Locate every Plasmodium ovale-infected red blood cell.
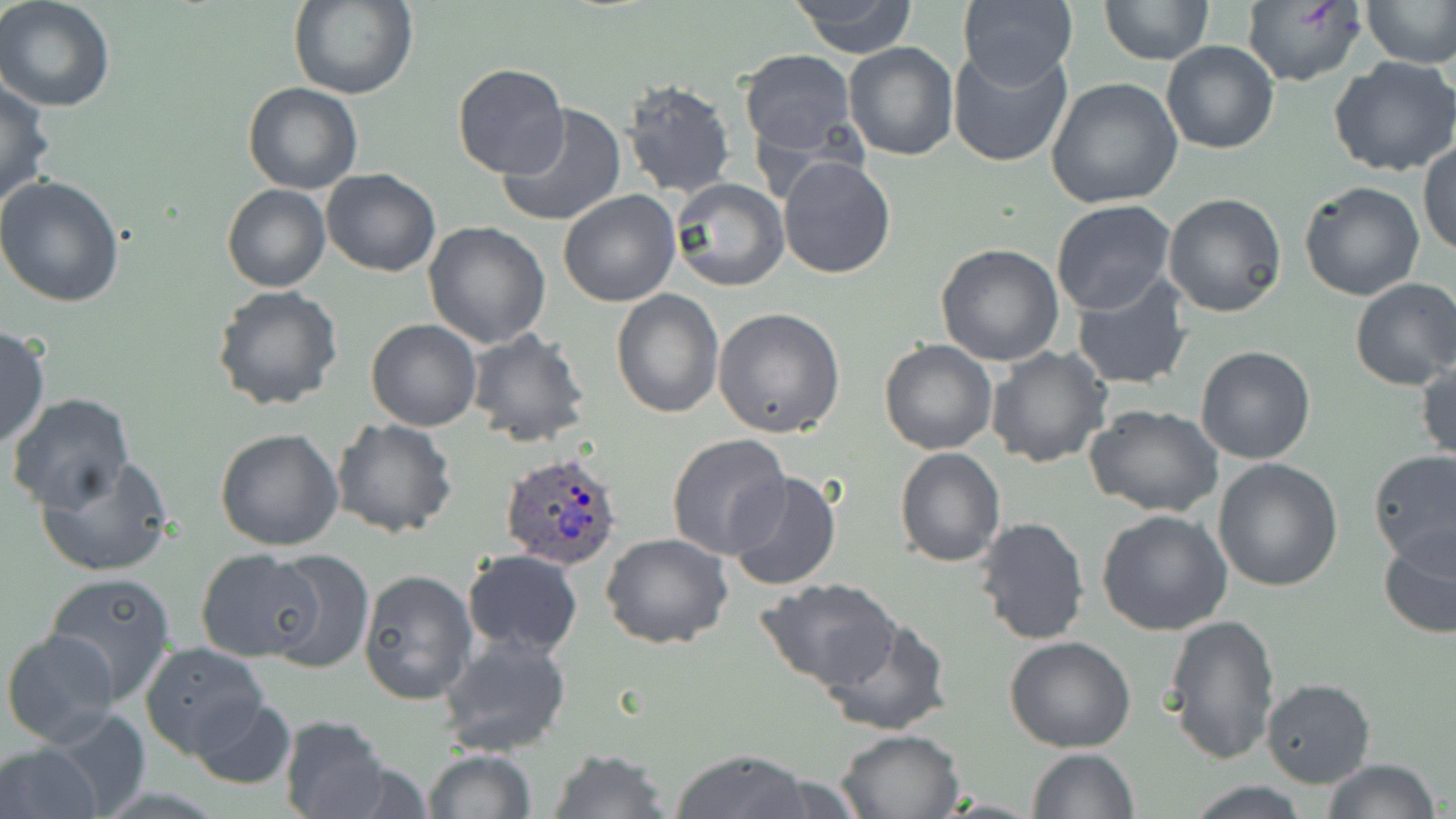

Approximate bounding boxes as (x1,y1)-(x2,y2) corner pairs in pixels.
Plasmodium ovale-infected red blood cells: (499,450)-(625,568).

slide_level_diagnosis: Plasmodium ovale
field_of_view: one of a larger specimen
preparation: thin blood smear
magnification: 1000x
stain: May-Grünwald-Giemsa
uninfected_red_blood_cell_locations: 'approximate bounding boxes as (x1,y1)-(x2,y2) corner pairs in pixels: (287,0)-(419,100), (790,0)-(919,56), (1100,0)-(1215,66), (1241,0)-(1365,86), (1365,0)-(1456,68), (0,1)-(118,113), (955,3)-(1078,84), (1161,38)-(1279,156), (843,42)-(960,161), (948,44)-(1075,168), (739,48)-(858,157), (1328,56)-(1456,176), (451,63)-(570,180), (1045,77)-(1186,209), (0,78)-(55,214), (618,78)-(737,199), (243,83)-(363,195), (496,103)-(627,228), (1419,140)-(1456,257), (777,154)-(896,279), (320,168)-(441,277), (0,173)-(126,307), (670,179)-(789,293), (1298,181)-(1425,300), (222,184)-(330,293), (558,189)-(682,307), (1162,192)-(1288,318), (1050,199)-(1178,316), (423,223)-(551,348), (935,242)-(1066,367), (1070,270)-(1196,391), (1349,278)-(1456,390), (212,285)-(346,411), (611,289)-(722,417), (713,308)-(845,438), (365,319)-(483,431), (0,324)-(49,451), (465,327)-(591,449), (879,339)-(998,455), (984,346)-(1112,468), (1194,346)-(1318,464), (1417,359)-(1455,465), (5,394)-(135,514), (1084,403)-(1225,517), (329,416)-(457,538), (215,428)-(346,551), (666,432)-(792,559), (895,447)-(1006,567), (1368,448)-(1456,566), (35,457)-(174,578), (1213,457)-(1344,592), (724,471)-(845,591), (1096,509)-(1233,636), (974,515)-(1091,645), (1377,523)-(1456,641), (600,532)-(733,650), (196,549)-(324,661), (264,550)-(375,675), (461,550)-(583,657), (358,568)-(477,706), (43,571)-(176,702), (755,579)-(900,689), (1163,613)-(1282,766), (818,614)-(953,736), (2,629)-(123,746), (436,630)-(571,757), (1004,637)-(1135,754), (140,641)-(270,759), (1261,677)-(1377,787), (186,695)-(299,789), (32,710)-(150,811), (279,714)-(393,819), (834,727)-(965,818), (0,743)-(103,819), (1027,747)-(1138,818), (547,748)-(673,819), (671,748)-(810,819), (421,749)-(537,819), (1320,759)-(1441,819), (737,767)-(862,818), (1183,782)-(1316,816)'
image_size: 1456×819 pixels
modality: optical microscopy